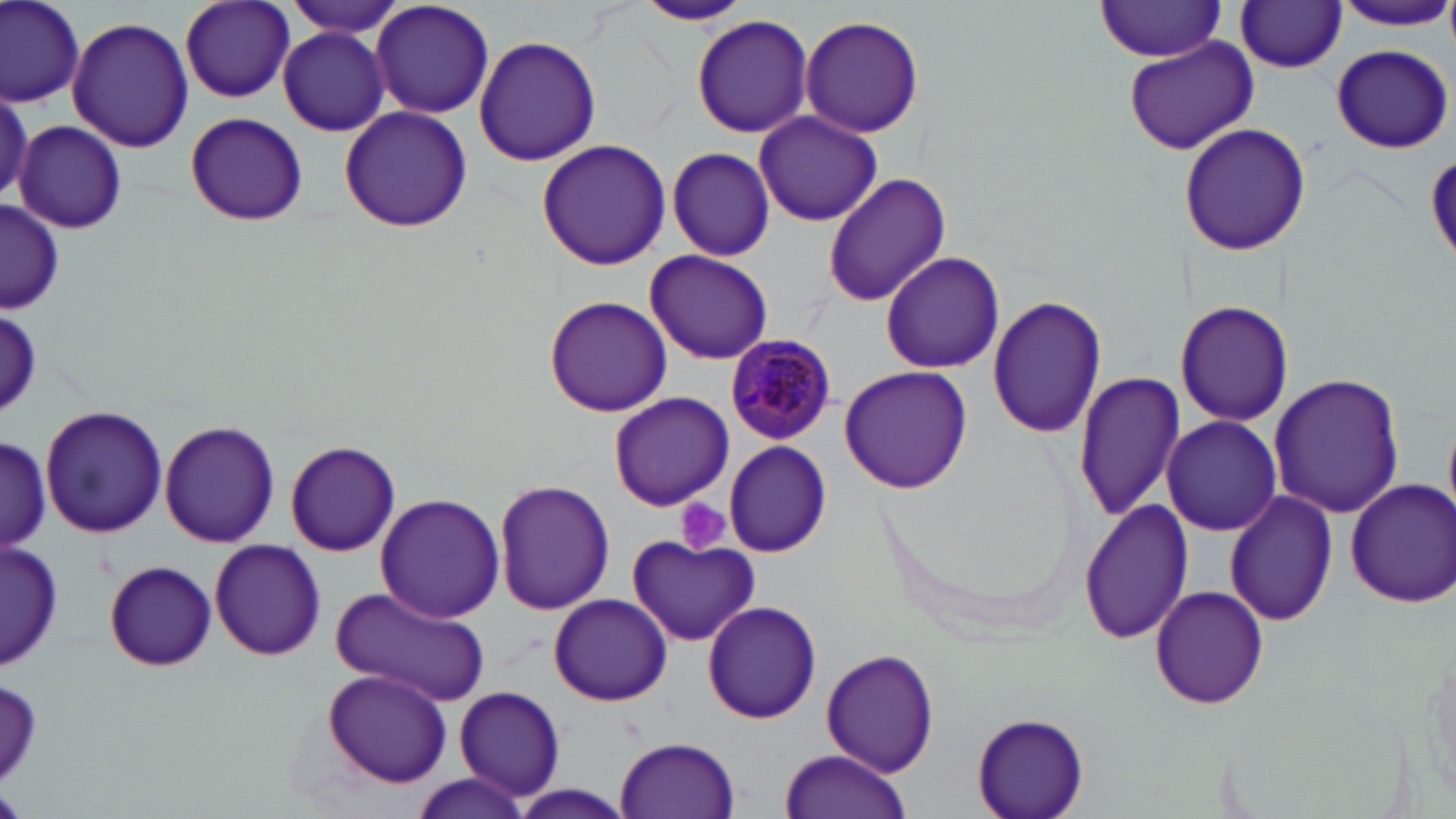

{
  "slide_level_diagnosis": "Plasmodium malariae",
  "modality": "optical microscopy",
  "uninfected_red_blood_cell_locations": "approximate bounding boxes as [x1, y1, x2, y2] in pixels: [1, 0, 84, 105], [180, 0, 295, 103], [282, 0, 409, 38], [371, 0, 495, 119], [1335, 0, 1454, 31], [634, 1, 755, 26], [1095, 1, 1228, 60], [1236, 2, 1348, 72], [800, 14, 924, 138], [691, 15, 813, 138], [67, 16, 193, 154], [279, 27, 390, 137], [474, 34, 601, 167], [1121, 34, 1260, 155], [1331, 44, 1455, 152], [0, 91, 32, 203], [339, 105, 473, 233], [185, 111, 308, 227], [755, 111, 883, 227], [16, 121, 126, 235], [1179, 123, 1309, 255], [537, 138, 671, 270], [663, 147, 775, 260], [823, 173, 951, 303], [0, 200, 63, 312], [644, 249, 773, 365], [880, 250, 1005, 374], [989, 294, 1105, 438], [544, 295, 672, 417], [1175, 300, 1292, 428], [2, 306, 42, 417], [839, 366, 972, 493], [1074, 369, 1185, 523], [1269, 373, 1403, 520], [609, 392, 734, 509], [39, 405, 168, 538], [1163, 415, 1282, 537], [160, 420, 280, 547], [0, 430, 51, 562], [284, 440, 401, 556], [722, 440, 832, 555], [493, 479, 615, 615], [1342, 479, 1456, 608], [1226, 491, 1337, 626], [375, 493, 505, 622], [1078, 498, 1194, 643], [628, 535, 763, 646], [1, 539, 61, 670], [208, 540, 327, 661], [104, 560, 217, 671], [1150, 585, 1269, 709], [331, 586, 491, 706], [549, 594, 672, 705], [701, 599, 824, 724], [1419, 640, 1455, 796], [821, 649, 940, 775], [321, 669, 452, 785], [455, 685, 566, 801], [972, 711, 1089, 819], [616, 735, 740, 818], [779, 750, 911, 819], [410, 774, 529, 818], [512, 784, 631, 817]",
  "plasmodium_malariae_infected_red_blood_cell_locations": "approximate bounding boxes as [x1, y1, x2, y2] in pixels: [724, 333, 834, 443]",
  "magnification": "1000x",
  "stain": "May-Grünwald-Giemsa",
  "platelet_locations": "approximate bounding boxes as [x1, y1, x2, y2] in pixels: [676, 499, 732, 556]",
  "image_size": "1456×819 pixels",
  "field_of_view": "one of a larger specimen",
  "preparation": "thin blood smear"
}